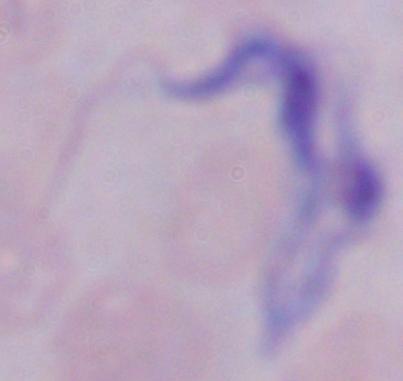
Captured at 1000x magnification. Micrograph. A trypanosome is shown.